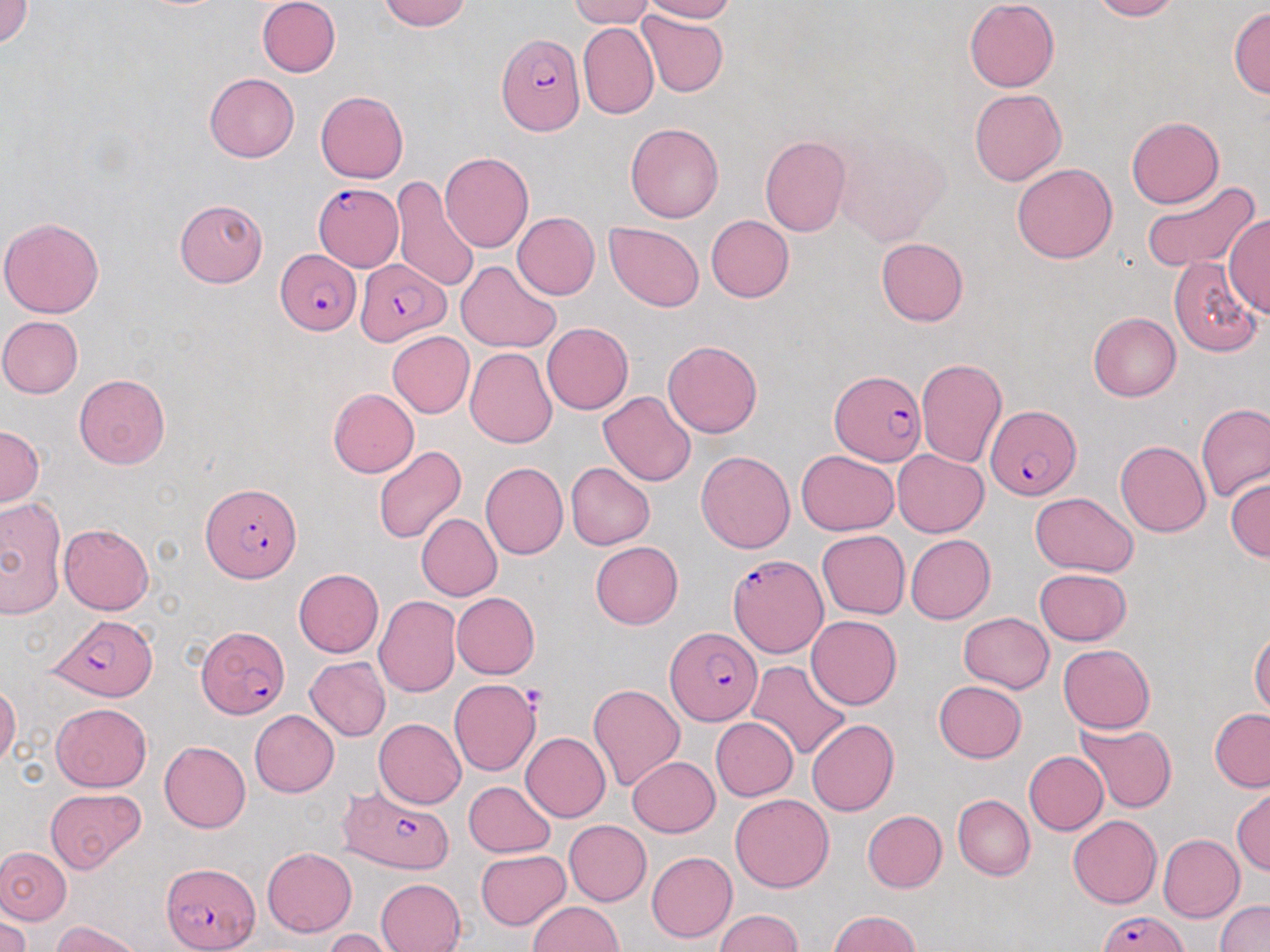 Approximate bounding boxes as (x1,y1)-(x2,y2) corner pairs in pixels. Plasmodium falciparum-infected red blood cell locations: (496,33)-(586,137), (315,183)-(403,270), (276,249)-(358,334), (354,260)-(451,345), (830,371)-(923,467), (985,406)-(1079,502), (202,482)-(301,581), (726,552)-(828,658), (48,615)-(160,702), (197,627)-(288,718), (665,627)-(761,726), (337,784)-(455,874), (162,863)-(259,950), (1097,909)-(1188,952). Platelet locations: (521,686)-(548,713). Uninfected red blood cell locations: (1,0)-(33,48), (256,0)-(340,77), (377,0)-(472,31), (568,0)-(655,28), (641,0)-(737,22), (965,0)-(1060,92), (1088,0)-(1181,21), (1229,6)-(1270,98), (635,9)-(730,98), (577,21)-(658,119), (204,73)-(299,163), (970,89)-(1066,186), (315,91)-(408,183), (1126,115)-(1224,208), (625,122)-(724,223), (836,130)-(952,247), (760,136)-(851,236), (440,152)-(534,253), (1012,163)-(1118,264), (391,177)-(481,292), (1139,180)-(1261,274), (174,198)-(267,288), (513,212)-(599,299), (1225,213)-(1269,319), (706,215)-(794,302), (0,216)-(104,319), (605,222)-(704,311), (876,238)-(969,326), (1169,257)-(1261,357), (456,261)-(561,353), (1088,312)-(1181,401), (0,315)-(84,398), (542,321)-(633,414), (388,331)-(475,418), (663,340)-(762,438), (465,347)-(557,449), (915,357)-(1007,467), (74,373)-(171,470), (328,388)-(419,477), (598,391)-(696,486), (1196,404)-(1269,500), (0,426)-(43,505), (1115,440)-(1211,537), (373,446)-(467,546), (697,450)-(795,553), (795,450)-(898,535), (892,450)-(988,537), (480,461)-(568,559), (566,462)-(655,549), (1226,475)-(1270,560), (1030,492)-(1138,577), (0,496)-(67,618), (416,513)-(502,600), (59,524)-(154,614), (817,530)-(909,619), (905,534)-(995,624), (591,541)-(683,628), (1035,568)-(1131,646), (293,569)-(384,657), (452,592)-(540,678), (373,596)-(461,697), (958,611)-(1053,694), (806,615)-(901,710), (1250,629)-(1270,717), (1058,644)-(1154,733), (305,658)-(391,741), (747,660)-(852,761), (449,679)-(541,776), (933,681)-(1026,763), (589,682)-(686,792), (0,684)-(21,769), (52,702)-(152,791), (1209,709)-(1270,792), (250,710)-(339,797), (710,717)-(798,800), (373,718)-(467,809), (806,718)-(899,816), (1073,722)-(1175,813), (521,732)-(611,822), (160,741)-(251,833), (1025,751)-(1108,835), (627,756)-(720,837), (464,780)-(556,858), (1232,787)-(1269,875), (45,788)-(146,872), (730,793)-(834,893), (953,795)-(1034,880), (862,810)-(947,893), (1068,814)-(1162,909), (564,819)-(651,905), (1158,834)-(1245,922), (0,847)-(72,923), (262,847)-(357,937), (476,848)-(570,928), (646,851)-(737,942), (376,878)-(466,952), (1215,900)-(1270,952), (528,901)-(623,951), (0,909)-(31,952), (714,909)-(802,951), (828,910)-(922,952), (54,921)-(142,952), (322,928)-(399,951). Slide-level diagnosis: Plasmodium falciparum. Captured at 1000x magnification. Single field of view. May-Grünwald-Giemsa-stained preparation. Thin blood smear. Optical microscopy. Image is 1270×952 pixels.